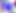
magnification = 400x
modality = photomicrograph
identification = Toxoplasma gondii